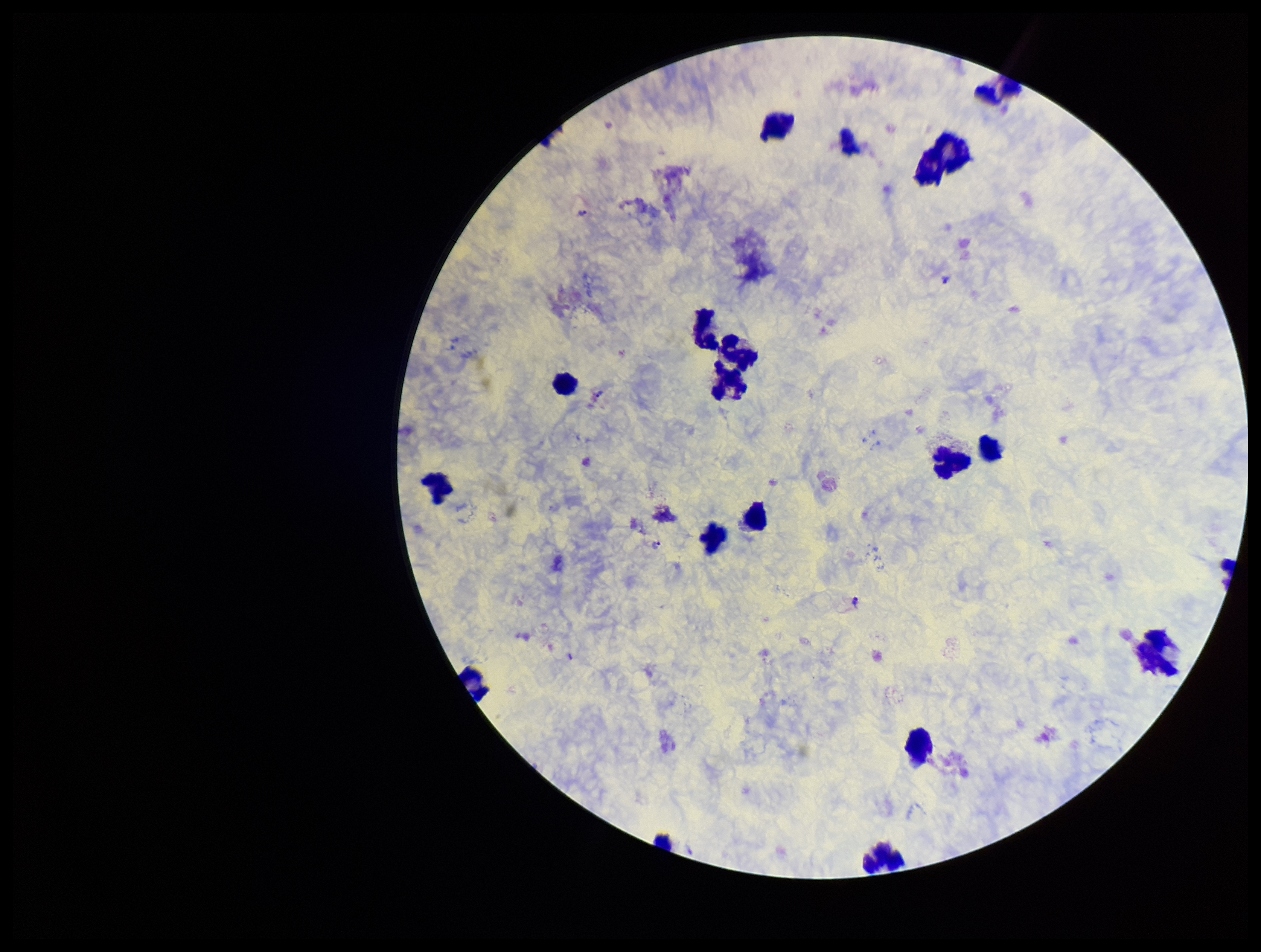

image size = 1261×952 pixels
preparation = thick blood smear
Plasmodium parasites = seen
capture = smartphone photograph through the microscope eyepiece
leukocyte count = 17
stain = Giemsa
species reported for this patient = Plasmodium vivax
field of view = one from this slide
parasite count = 4
patient malaria status = positive